Describe the morphology of the erythrocytes.
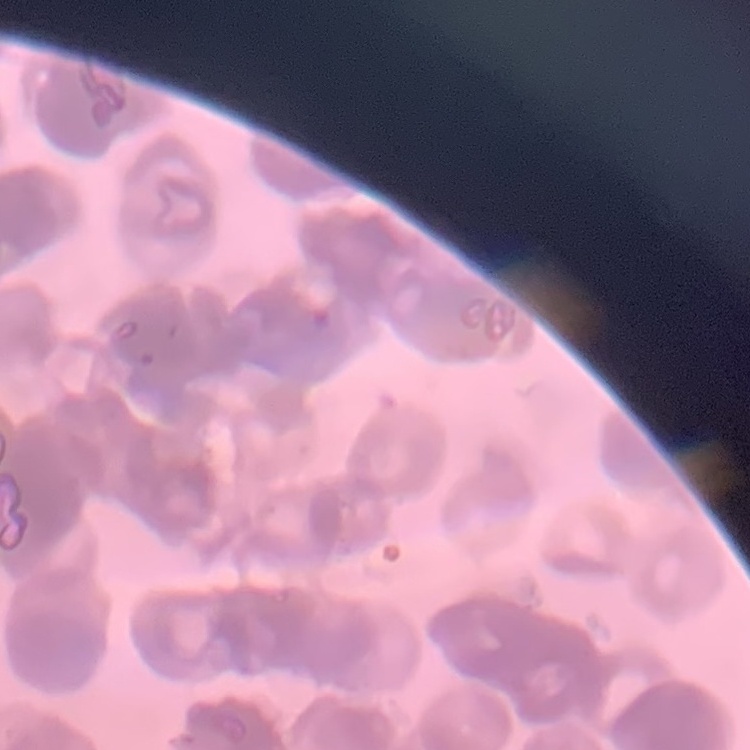
Rouleaux formation.

Summary:
  - Preparation: thin blood smear
  - Image type: square crop of a larger photomicrograph
  - Stain: Field's or Giemsa